Classify this cell by malaria status.
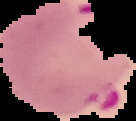
Parasitized.

Summary:
  - Image type: segmented cell region on a black background
  - Preparation: thin blood smear
  - Image size: 136×121 pixels